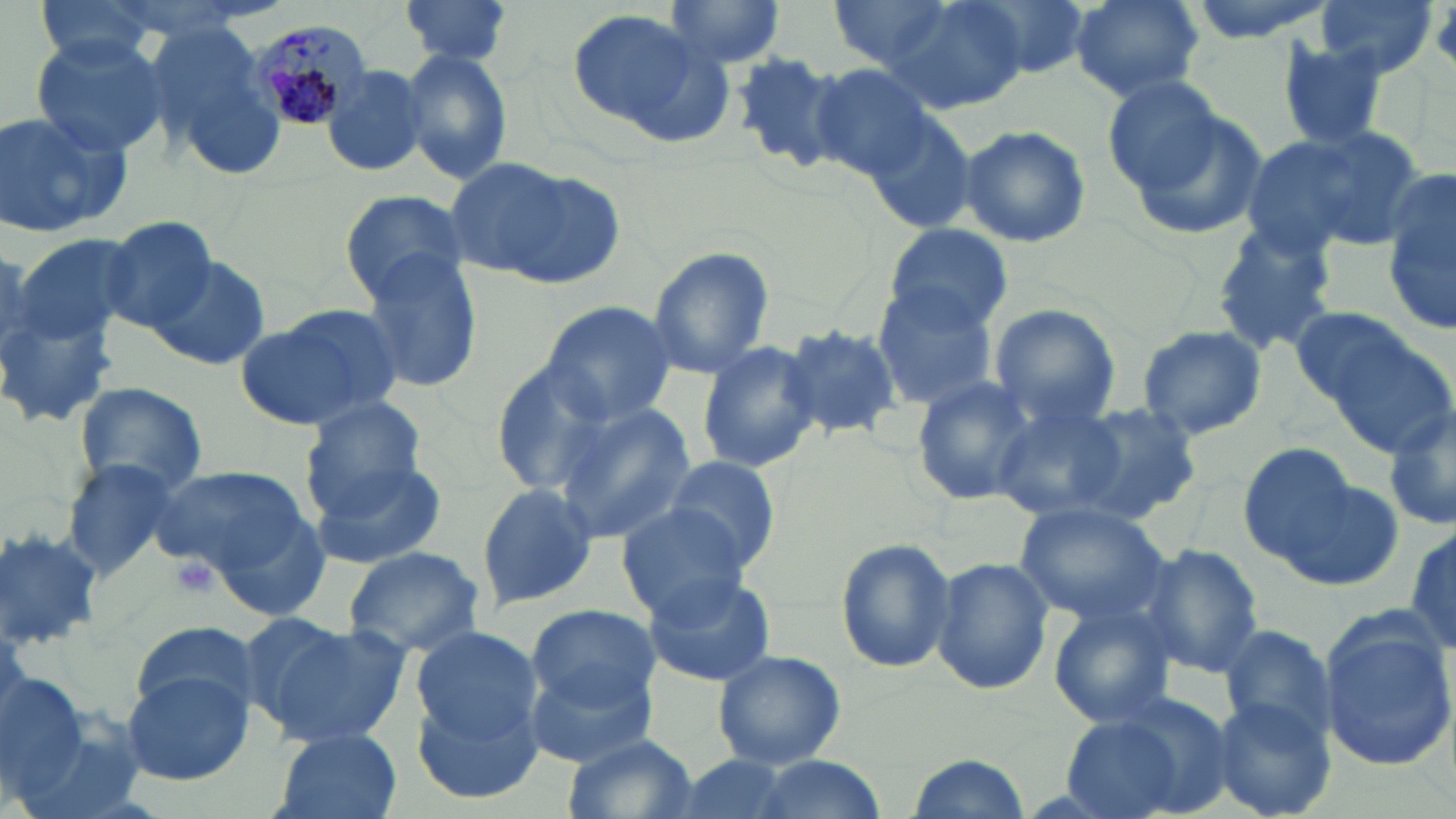

slide_level_diagnosis: Plasmodium malariae
image_size: 1456×819 pixels
platelet_locations: 'approximate bounding boxes as (x1, y1, x2, y2) in pixels: (168, 556, 222, 601)'
modality: light microscopy
field_of_view: single
preparation: thin blood smear
plasmodium_malariae_infected_red_blood_cell_locations: 'approximate bounding boxes as (x1, y1, x2, y2) in pixels: (249, 17, 374, 134)'
magnification: 1000x
uninfected_red_blood_cell_locations: 'approximate bounding boxes as (x1, y1, x2, y2) in pixels: (32, 0, 166, 74), (661, 0, 789, 71), (883, 0, 1026, 115), (968, 0, 1095, 79), (1068, 0, 1204, 102), (1312, 0, 1437, 79), (402, 1, 511, 68), (826, 1, 962, 70), (567, 9, 727, 143), (147, 20, 286, 177), (30, 35, 166, 158), (1275, 39, 1393, 149), (399, 49, 514, 184), (727, 50, 849, 172), (805, 64, 938, 182), (321, 65, 431, 179), (1100, 73, 1231, 195), (1122, 102, 1268, 245), (0, 108, 130, 238), (864, 115, 979, 235), (1246, 123, 1426, 257), (956, 124, 1091, 248), (442, 158, 585, 280), (1384, 165, 1456, 335), (337, 188, 470, 303), (97, 218, 218, 333), (883, 224, 1014, 334), (1210, 224, 1343, 354), (647, 246, 775, 380), (359, 253, 484, 394), (150, 255, 271, 370), (0, 270, 125, 436), (871, 285, 999, 410), (539, 301, 680, 426), (988, 304, 1122, 426), (237, 306, 403, 433), (1301, 311, 1455, 455), (779, 323, 903, 441), (1136, 325, 1269, 440), (696, 339, 820, 474), (493, 359, 618, 495), (910, 376, 1038, 504), (73, 380, 210, 495), (301, 396, 431, 506), (1040, 399, 1207, 526), (551, 403, 697, 542), (992, 405, 1134, 521), (1384, 409, 1456, 535), (1238, 441, 1363, 568), (657, 453, 782, 572), (63, 458, 184, 576), (312, 459, 447, 571), (1271, 465, 1405, 590), (150, 466, 314, 580), (476, 483, 597, 611), (614, 503, 754, 625), (1014, 503, 1170, 626), (216, 514, 328, 618), (1406, 524, 1456, 655), (836, 536, 957, 674), (1136, 543, 1267, 679), (340, 546, 485, 656), (930, 557, 1054, 695), (642, 572, 776, 687), (1047, 604, 1178, 729), (525, 605, 655, 716), (1317, 615, 1456, 771), (254, 617, 409, 749), (130, 619, 259, 721), (1218, 622, 1336, 746), (408, 623, 544, 747), (521, 647, 659, 767), (712, 648, 847, 768), (119, 669, 256, 787), (0, 671, 88, 800), (412, 687, 546, 804), (1205, 695, 1335, 819), (1060, 697, 1229, 819), (269, 727, 404, 819), (562, 731, 696, 819), (735, 754, 894, 819), (904, 754, 1029, 817)'
stain: May-Grünwald-Giemsa